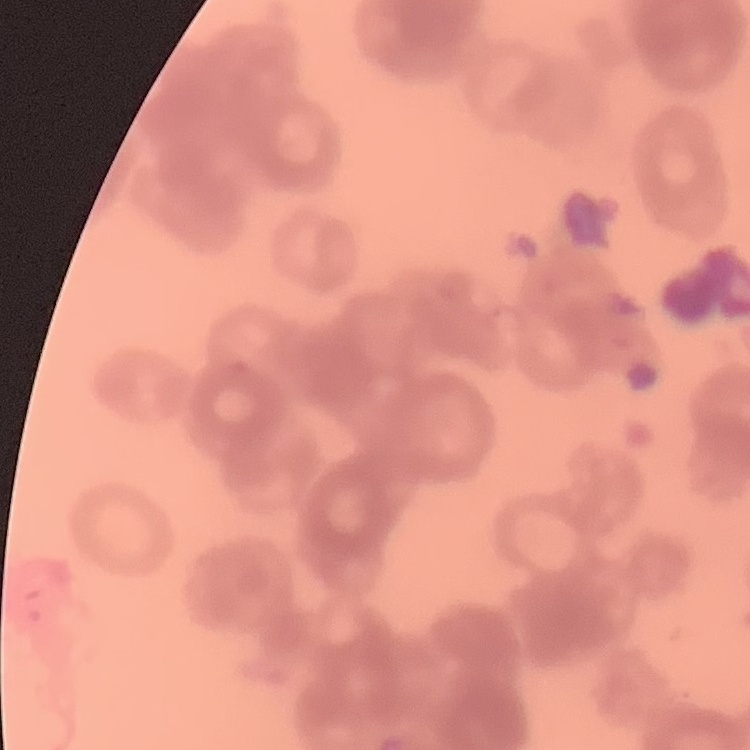

Summary:
  - Red blood cell morphology: rouleaux formation
  - Preparation: thin blood smear
  - Image type: one tile cut from a larger photomicrograph
  - Stain: Field's or Giemsa